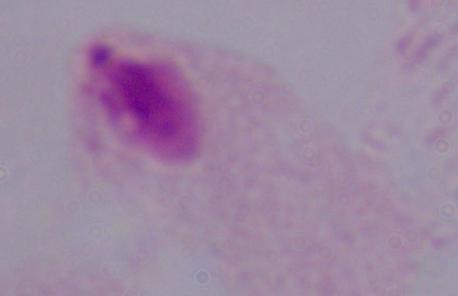
identification = trichomonad
modality = micrograph
magnification = 1000x